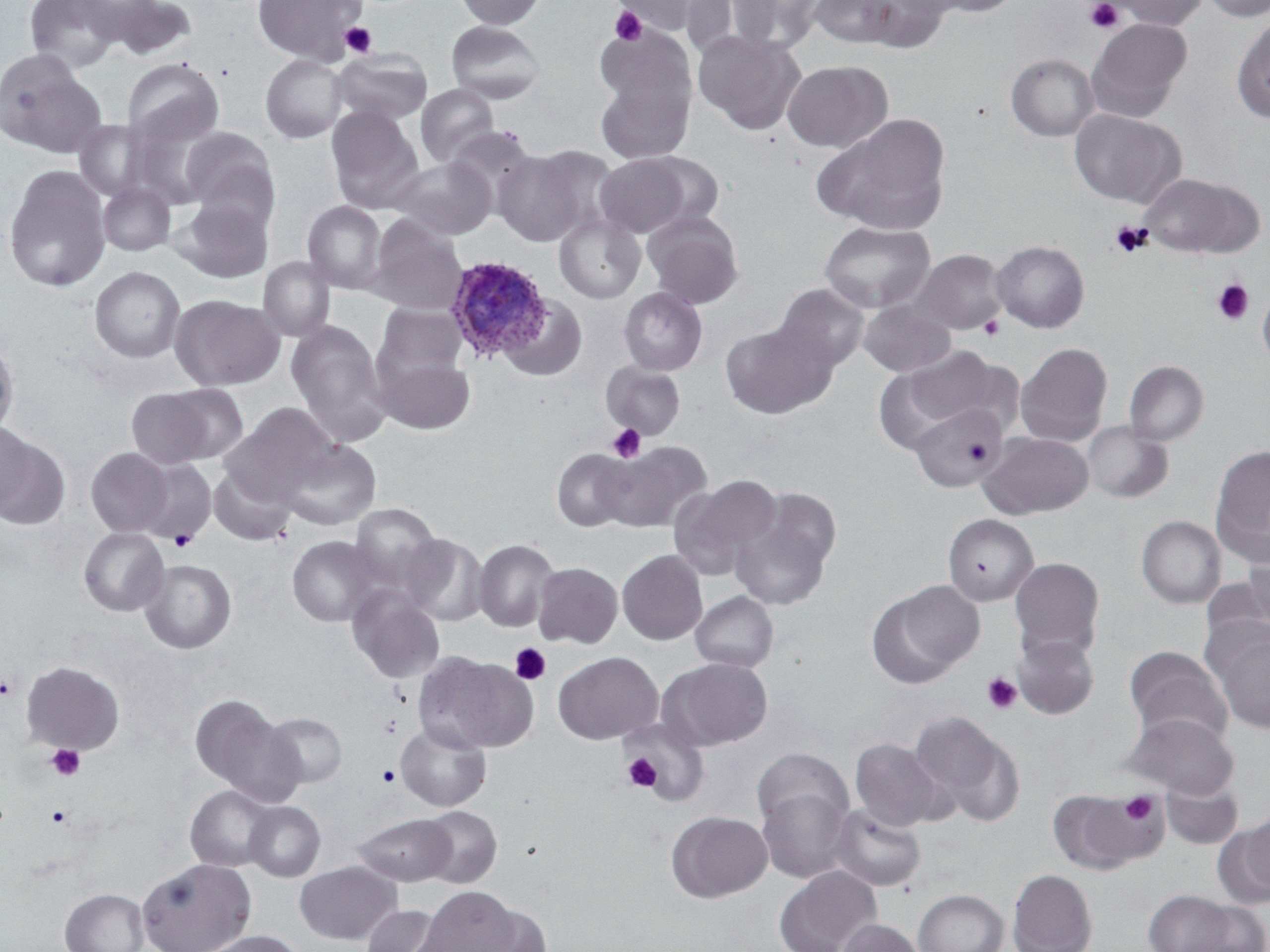

Approximate bounding boxes as named x1/y1/x2/y2 corners in pixels. Platelet locations: (x1=1085, y1=0, x2=1125, y2=35), (x1=609, y1=5, x2=648, y2=46), (x1=339, y1=22, x2=377, y2=58), (x1=1109, y1=221, x2=1150, y2=257), (x1=1212, y1=278, x2=1254, y2=325), (x1=979, y1=316, x2=1005, y2=340), (x1=606, y1=423, x2=647, y2=463), (x1=971, y1=444, x2=989, y2=462), (x1=169, y1=529, x2=197, y2=551), (x1=509, y1=643, x2=550, y2=686), (x1=981, y1=673, x2=1022, y2=715), (x1=1, y1=674, x2=19, y2=701), (x1=378, y1=715, x2=401, y2=738), (x1=46, y1=743, x2=85, y2=782), (x1=622, y1=753, x2=661, y2=792), (x1=377, y1=765, x2=400, y2=786), (x1=1118, y1=791, x2=1163, y2=828), (x1=46, y1=805, x2=71, y2=828). Plasmodium ovale-infected red blood cell locations: (x1=444, y1=252, x2=554, y2=362). Uninfected red blood cell locations: (x1=25, y1=0, x2=123, y2=72), (x1=71, y1=0, x2=172, y2=46), (x1=103, y1=0, x2=197, y2=60), (x1=252, y1=0, x2=367, y2=64), (x1=454, y1=0, x2=547, y2=30), (x1=612, y1=0, x2=712, y2=36), (x1=682, y1=0, x2=779, y2=60), (x1=730, y1=0, x2=827, y2=52), (x1=808, y1=0, x2=903, y2=49), (x1=853, y1=0, x2=951, y2=53), (x1=916, y1=0, x2=1024, y2=18), (x1=1110, y1=0, x2=1209, y2=30), (x1=1199, y1=0, x2=1270, y2=22), (x1=1232, y1=15, x2=1270, y2=123), (x1=1085, y1=18, x2=1191, y2=123), (x1=445, y1=20, x2=546, y2=104), (x1=595, y1=24, x2=695, y2=113), (x1=693, y1=29, x2=805, y2=136), (x1=331, y1=48, x2=433, y2=126), (x1=0, y1=52, x2=106, y2=157), (x1=1005, y1=53, x2=1099, y2=142), (x1=260, y1=54, x2=348, y2=143), (x1=121, y1=57, x2=224, y2=149), (x1=782, y1=60, x2=892, y2=153), (x1=595, y1=72, x2=694, y2=163), (x1=415, y1=84, x2=500, y2=168), (x1=325, y1=107, x2=424, y2=213), (x1=1069, y1=108, x2=1187, y2=207), (x1=129, y1=111, x2=224, y2=209), (x1=814, y1=114, x2=952, y2=236), (x1=74, y1=120, x2=149, y2=200), (x1=446, y1=125, x2=538, y2=213), (x1=179, y1=126, x2=280, y2=224), (x1=492, y1=148, x2=594, y2=246), (x1=639, y1=152, x2=726, y2=229), (x1=594, y1=154, x2=694, y2=237), (x1=391, y1=156, x2=497, y2=239), (x1=3, y1=163, x2=111, y2=293), (x1=1139, y1=173, x2=1265, y2=258), (x1=97, y1=182, x2=176, y2=257), (x1=173, y1=196, x2=275, y2=283), (x1=302, y1=201, x2=387, y2=294), (x1=642, y1=211, x2=744, y2=309), (x1=554, y1=213, x2=646, y2=304), (x1=367, y1=215, x2=468, y2=315), (x1=819, y1=220, x2=935, y2=313), (x1=991, y1=240, x2=1090, y2=333), (x1=911, y1=249, x2=1008, y2=335), (x1=257, y1=256, x2=335, y2=342), (x1=89, y1=265, x2=186, y2=363), (x1=773, y1=284, x2=869, y2=373), (x1=1257, y1=284, x2=1270, y2=369), (x1=618, y1=287, x2=708, y2=376), (x1=169, y1=294, x2=284, y2=391), (x1=500, y1=295, x2=588, y2=382), (x1=858, y1=300, x2=957, y2=376), (x1=373, y1=303, x2=466, y2=382), (x1=286, y1=320, x2=391, y2=445), (x1=721, y1=320, x2=836, y2=420), (x1=0, y1=341, x2=19, y2=438), (x1=1015, y1=343, x2=1113, y2=447), (x1=899, y1=346, x2=1009, y2=429), (x1=372, y1=352, x2=476, y2=435), (x1=1124, y1=361, x2=1209, y2=446), (x1=600, y1=362, x2=686, y2=440), (x1=161, y1=384, x2=249, y2=464), (x1=125, y1=388, x2=215, y2=468), (x1=223, y1=402, x2=337, y2=498), (x1=909, y1=404, x2=1009, y2=491), (x1=1082, y1=421, x2=1173, y2=503), (x1=1, y1=422, x2=35, y2=512), (x1=0, y1=431, x2=70, y2=530), (x1=979, y1=431, x2=1094, y2=519), (x1=277, y1=439, x2=381, y2=531), (x1=602, y1=441, x2=712, y2=533), (x1=1210, y1=445, x2=1270, y2=565), (x1=85, y1=448, x2=174, y2=536), (x1=550, y1=448, x2=634, y2=532), (x1=135, y1=458, x2=217, y2=544), (x1=208, y1=465, x2=296, y2=546), (x1=668, y1=477, x2=782, y2=580), (x1=729, y1=497, x2=837, y2=610), (x1=348, y1=503, x2=442, y2=591), (x1=942, y1=513, x2=1039, y2=606), (x1=1136, y1=515, x2=1226, y2=608), (x1=78, y1=527, x2=168, y2=616), (x1=399, y1=533, x2=488, y2=626), (x1=286, y1=535, x2=383, y2=627), (x1=473, y1=539, x2=559, y2=632), (x1=1242, y1=541, x2=1270, y2=635), (x1=617, y1=549, x2=707, y2=645), (x1=1009, y1=557, x2=1105, y2=659), (x1=139, y1=559, x2=237, y2=654), (x1=532, y1=562, x2=623, y2=648), (x1=869, y1=583, x2=981, y2=686), (x1=346, y1=585, x2=446, y2=684), (x1=690, y1=591, x2=779, y2=672), (x1=1212, y1=630, x2=1270, y2=734), (x1=1012, y1=633, x2=1099, y2=719), (x1=1124, y1=646, x2=1232, y2=744), (x1=553, y1=651, x2=663, y2=744), (x1=416, y1=653, x2=538, y2=755), (x1=667, y1=658, x2=772, y2=750), (x1=20, y1=660, x2=125, y2=755), (x1=190, y1=694, x2=301, y2=803), (x1=908, y1=711, x2=1021, y2=824), (x1=262, y1=712, x2=348, y2=788), (x1=1122, y1=712, x2=1239, y2=798), (x1=623, y1=718, x2=708, y2=804), (x1=395, y1=722, x2=491, y2=812), (x1=850, y1=739, x2=946, y2=830), (x1=752, y1=747, x2=853, y2=832), (x1=1161, y1=775, x2=1242, y2=849), (x1=185, y1=784, x2=278, y2=872), (x1=757, y1=787, x2=853, y2=883), (x1=1049, y1=788, x2=1161, y2=874), (x1=243, y1=801, x2=326, y2=882), (x1=419, y1=805, x2=503, y2=888), (x1=828, y1=805, x2=926, y2=891), (x1=666, y1=811, x2=772, y2=902), (x1=1224, y1=812, x2=1269, y2=904), (x1=352, y1=813, x2=456, y2=886), (x1=137, y1=857, x2=255, y2=952), (x1=295, y1=861, x2=401, y2=945), (x1=775, y1=865, x2=882, y2=952), (x1=1007, y1=869, x2=1097, y2=952), (x1=418, y1=886, x2=521, y2=952), (x1=60, y1=888, x2=149, y2=952), (x1=1143, y1=888, x2=1254, y2=952), (x1=913, y1=889, x2=1009, y2=952), (x1=466, y1=902, x2=553, y2=952), (x1=361, y1=905, x2=447, y2=952), (x1=837, y1=918, x2=925, y2=952), (x1=199, y1=930, x2=307, y2=952). Slide-level diagnosis: Plasmodium ovale. Thin blood smear. 1000x magnification. Optical microscopy. Image is 1270×952 pixels. May-Grünwald-Giemsa-stained preparation. One field of a larger specimen.